Locate every uninfected red blood cell.
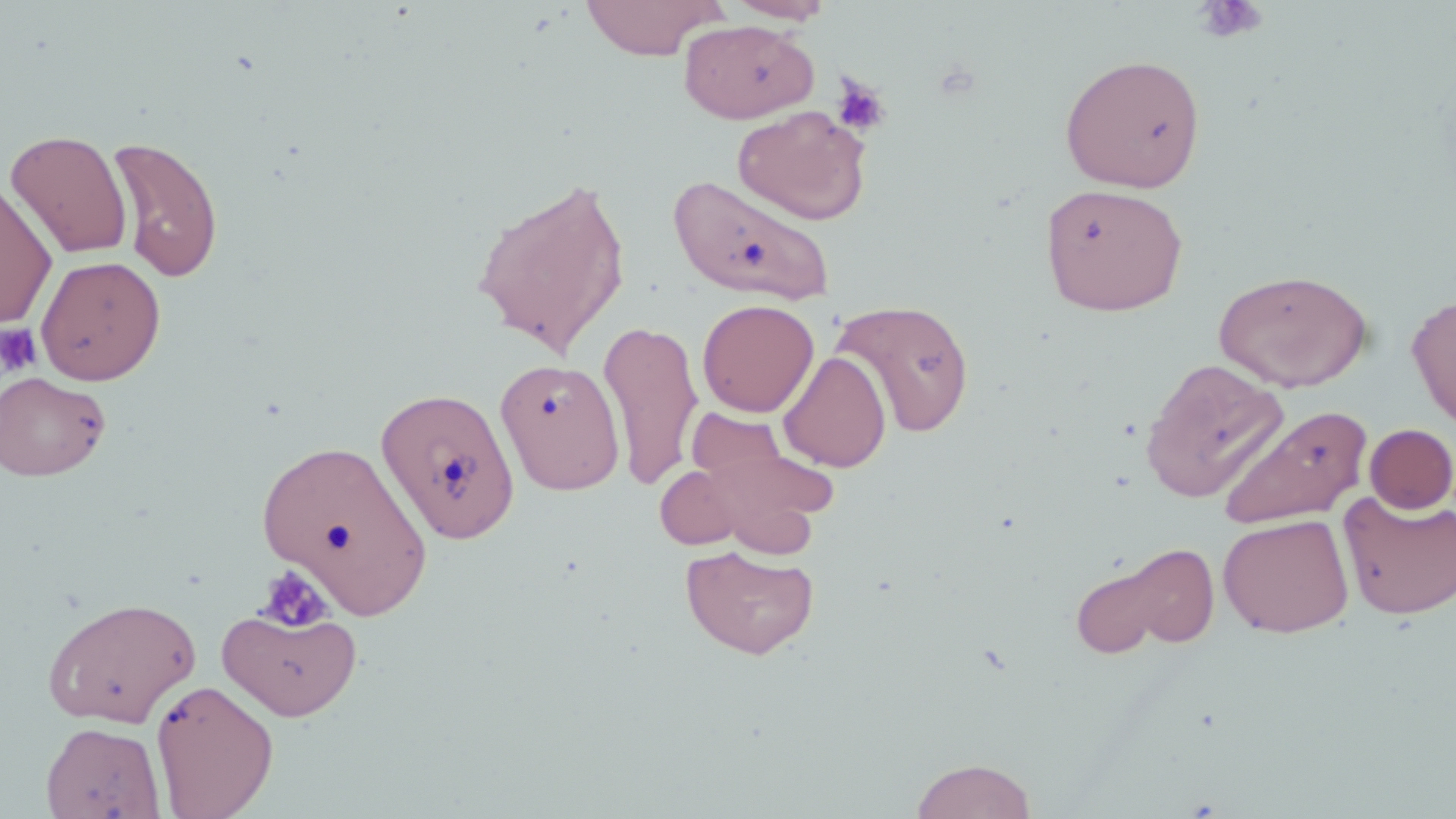
Approximate bounding boxes as (x1,y1)-(x2,y2) corner pairs in pixels.
Uninfected red blood cells: (580,0)-(726,60), (725,0)-(836,24), (678,19)-(818,123), (1059,53)-(1206,192), (733,106)-(871,225), (5,129)-(133,260), (107,136)-(225,283), (668,172)-(836,306), (471,173)-(632,359), (0,179)-(58,329), (1039,183)-(1188,316), (35,255)-(166,385), (1214,268)-(1373,392), (1406,294)-(1456,432), (697,298)-(819,417), (830,298)-(976,438), (599,319)-(703,489), (778,351)-(892,473), (494,358)-(626,495), (1139,358)-(1289,503), (0,371)-(110,481), (375,386)-(519,542), (1218,405)-(1372,531), (685,406)-(794,494), (1364,424)-(1456,514), (692,434)-(837,556), (257,438)-(433,618), (654,465)-(748,550), (1338,491)-(1456,620), (1218,513)-(1354,637), (680,544)-(820,660), (1069,545)-(1213,659), (41,596)-(201,728), (217,602)-(362,721), (150,678)-(279,818), (41,721)-(165,819), (911,757)-(1038,819).

Summary:
  - Platelet locations: (1193,1)-(1268,43), (831,75)-(890,137), (0,324)-(41,376), (255,565)-(335,634)
  - Slide-level diagnosis: negative for blood parasites
  - Stain: May-Grünwald-Giemsa
  - Magnification: 1000x
  - Modality: optical microscopy
  - Image size: 1456×819 pixels
  - Preparation: thin blood film
  - Field of view: one of a larger specimen